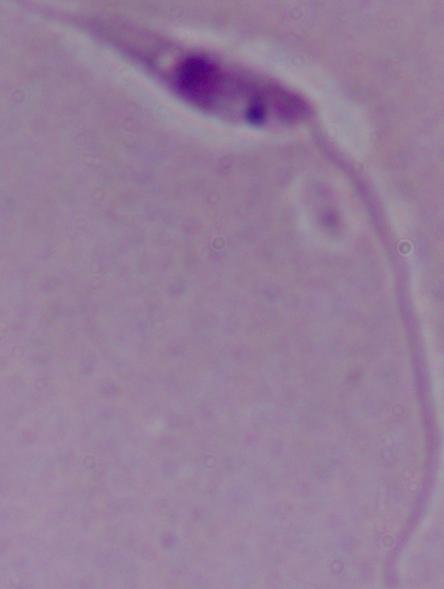

Summary:
  - Modality: micrograph
  - Identification: Leishmania
  - Magnification: 1000x